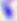
Summary:
  - Modality: micrograph
  - Magnification: 400x
  - Identification: Toxoplasma gondii